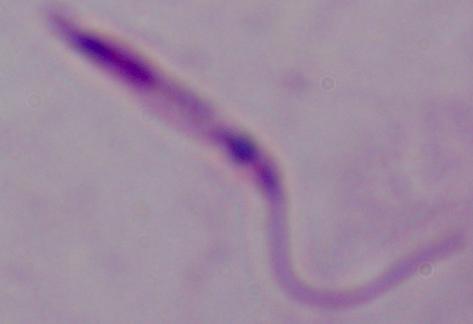
modality = photomicrograph
identification = Leishmania
magnification = 1000x